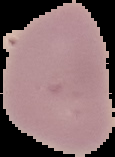
image size = 115×157 pixels
image type = segmented cell region on a black background
result = no Plasmodium parasites seen
preparation = thin blood film